Identify the cell.
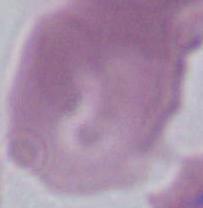

An erythrocyte.

Summary:
  - Modality: photomicrograph
  - Magnification: 1000x